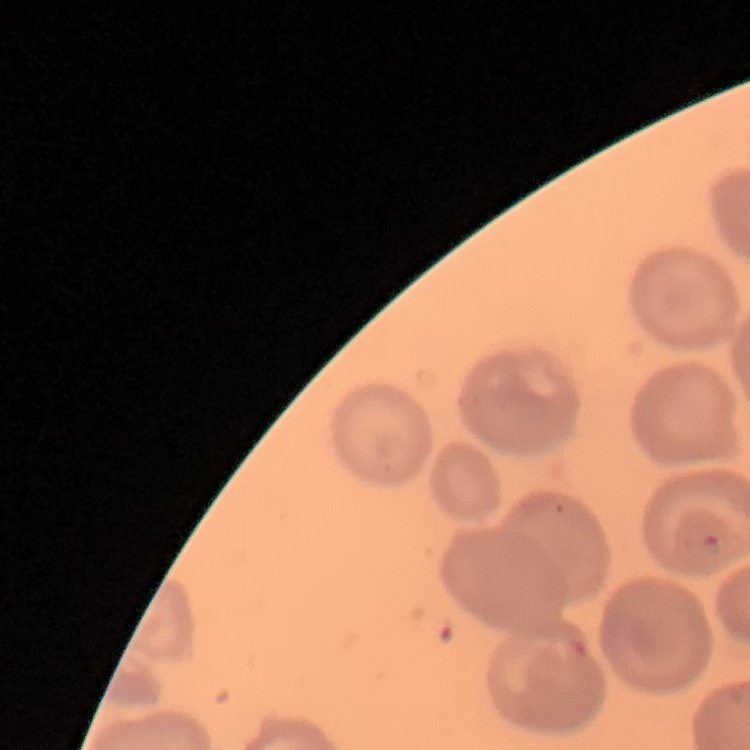

{
  "red_blood_cell_morphology": "no rouleaux formation",
  "stain": "Field's or Giemsa",
  "image_type": "square crop of a larger photomicrograph",
  "preparation": "thin blood film"
}